Point out malaria parasites and leukocytes.
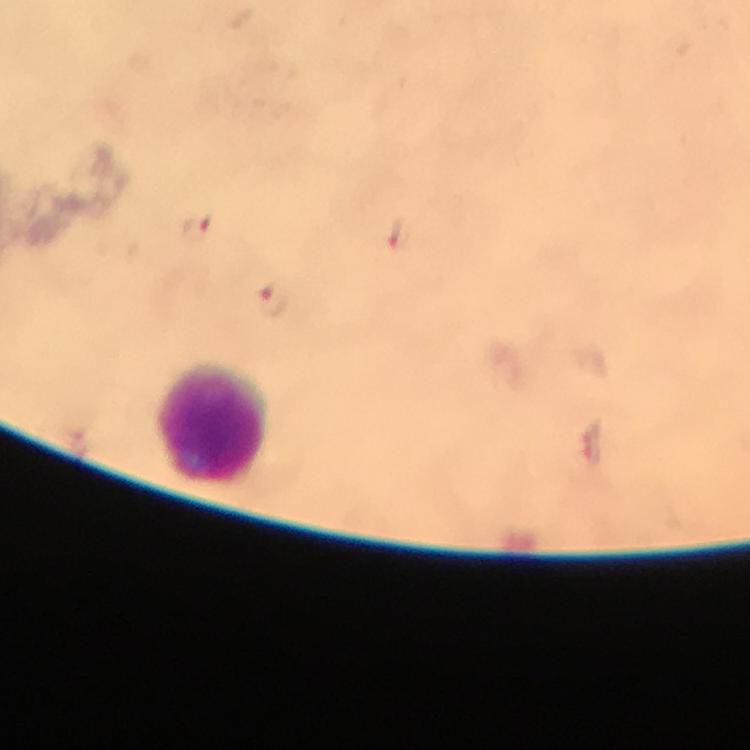
Approximate object centers, in pixels from the top-left corner.
Malaria parasites: (x=197, y=227), (x=398, y=233), (x=274, y=299), (x=591, y=446).
Leukocytes: (x=212, y=424).

A crop from one field of view. Thick smear. Image is 750×750 pixels. Immersion oil applied. From a diagnostic examination for malaria. Giemsa stain. Photographed with a smartphone mounted on the microscope. At 100x magnification.